Classify this cell by malaria status.
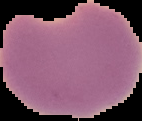

It is parasitized.

The area outside the segmented cell region is set to black. From a thin blood film. Image is 142×121 pixels.